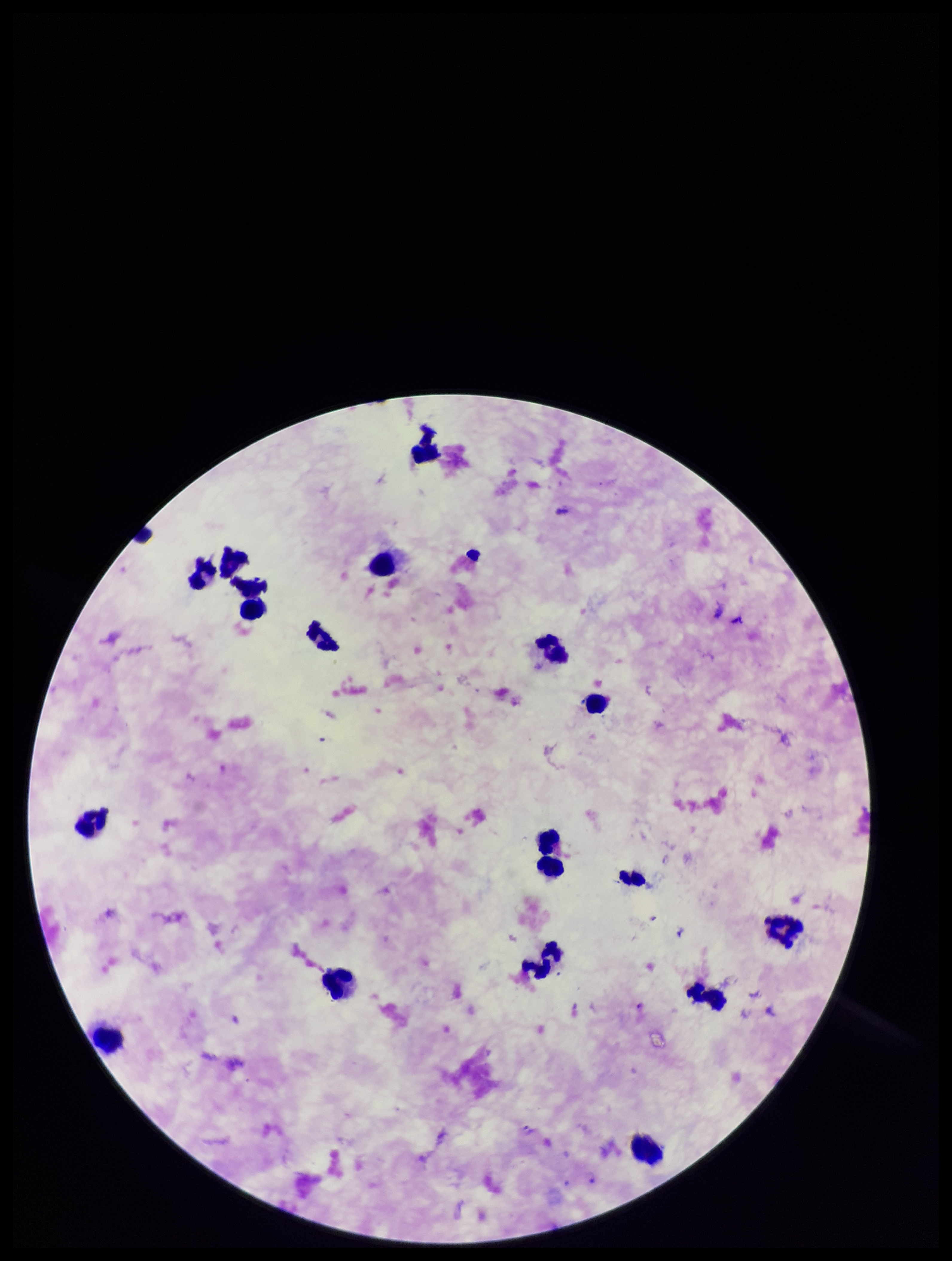
Summary:
  - Species reported for this patient: Plasmodium falciparum
  - Patient malaria status: infected
  - Plasmodium parasites: identified
  - Field of view: single
  - Parasite count: 1
  - Leukocyte count: 20
  - Preparation: thick
  - Image size: 952×1261 pixels
  - Capture: smartphone photograph through the microscope eyepiece
  - Stain: Giemsa